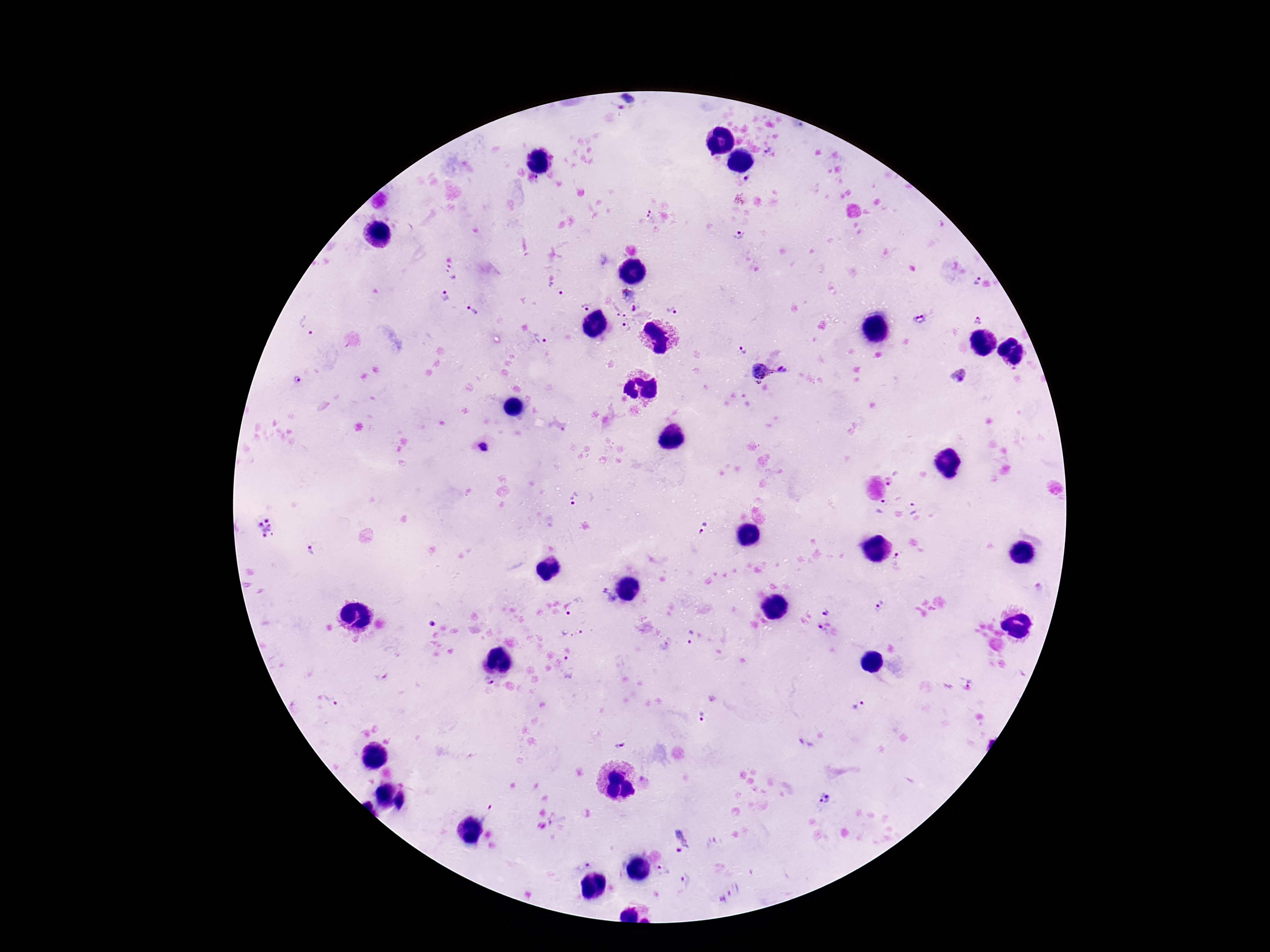

preparation = thick blood film
image size = 1270×952 pixels
magnification = 100x
capture = smartphone camera through the microscope eyepiece
field of view = one from this slide
stain = Giemsa
Plasmodium parasite locations = approximate object centers, in pixels from the top-left corner: (x=625, y=102), (x=768, y=151), (x=746, y=179), (x=740, y=200), (x=647, y=217), (x=739, y=235), (x=451, y=273), (x=976, y=281), (x=556, y=288), (x=627, y=294), (x=445, y=297), (x=585, y=306), (x=472, y=310), (x=673, y=310), (x=626, y=316), (x=920, y=320), (x=978, y=320), (x=310, y=326), (x=541, y=337), (x=742, y=352), (x=770, y=375), (x=959, y=375), (x=297, y=381), (x=485, y=448), (x=892, y=482), (x=575, y=498), (x=881, y=506), (x=913, y=508), (x=266, y=528), (x=704, y=529), (x=310, y=552), (x=897, y=559), (x=1039, y=587), (x=606, y=598), (x=878, y=603), (x=577, y=607), (x=825, y=611), (x=432, y=624), (x=822, y=632), (x=573, y=633), (x=689, y=636), (x=572, y=666), (x=969, y=677), (x=488, y=682), (x=331, y=700), (x=861, y=705), (x=702, y=717), (x=618, y=742), (x=825, y=799), (x=489, y=812), (x=556, y=818), (x=679, y=840), (x=583, y=863), (x=664, y=871), (x=688, y=882)
patient malaria status = positive